Describe the morphology of the red blood cells.
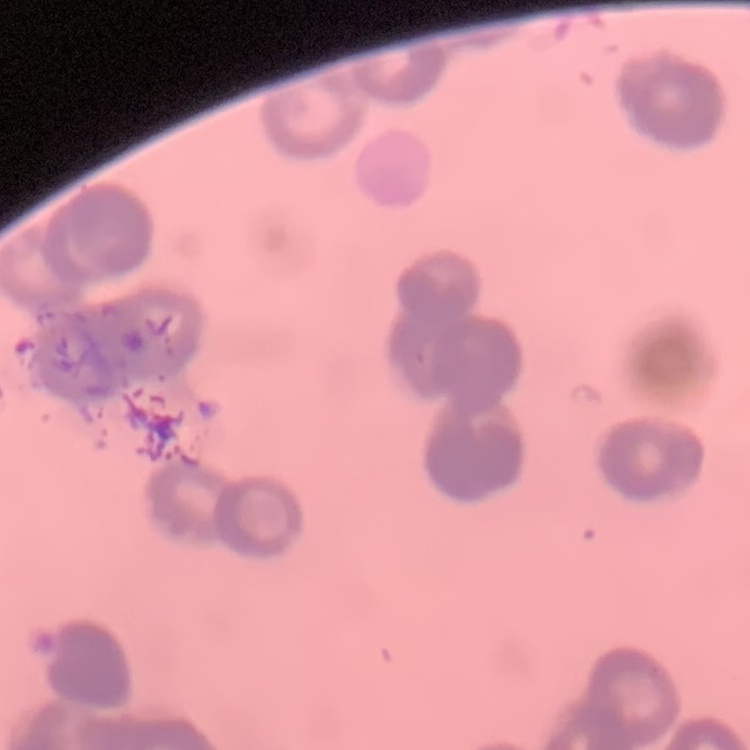
They show rouleaux formation.

preparation = thin blood film
image type = square crop of a larger photomicrograph
stain = Field's or Giemsa